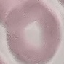
Result: no malaria parasites seen. Photographed with a smartphone camera at the microscope eyepiece. Cell patch, automatically extracted from a larger field of view and resized to 64 × 64 pixels. Thin smear of blood. Giemsa-stained preparation.